Outline each blood parasite and name the species.
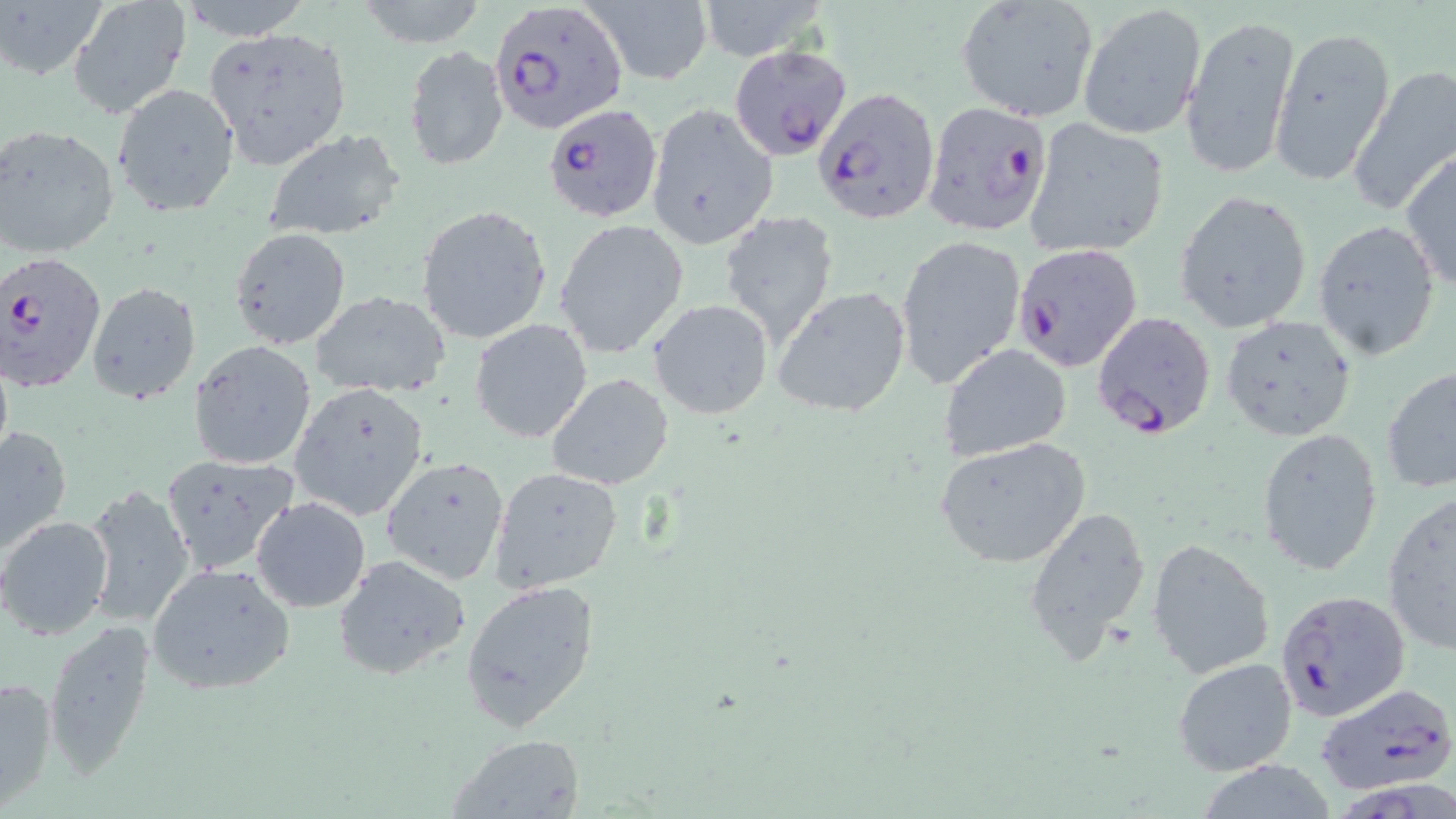

Approximate bounding boxes as named x1/y1/x2/y2 corners in pixels.
Plasmodium falciparum-infected red blood cells: (x1=492, y1=1, x2=628, y2=137), (x1=722, y1=42, x2=851, y2=167), (x1=811, y1=83, x2=941, y2=226), (x1=922, y1=99, x2=1054, y2=238), (x1=542, y1=104, x2=661, y2=222), (x1=1012, y1=242, x2=1143, y2=372), (x1=0, y1=251, x2=106, y2=393), (x1=1090, y1=310, x2=1217, y2=440), (x1=1275, y1=588, x2=1411, y2=722), (x1=1337, y1=771, x2=1456, y2=819).
No Plasmodium ovale, Plasmodium malariae, Plasmodium vivax, Babesia divergens, or Trypanosoma brucei observed.

slide-level diagnosis = Plasmodium falciparum
stain = May-Grünwald-Giemsa
magnification = 1000x
uninfected red blood cell locations = approximate bounding boxes as named x1/y1/x2/y2 corners in pixels: (x1=4, y1=0, x2=109, y2=82), (x1=67, y1=0, x2=192, y2=120), (x1=176, y1=0, x2=309, y2=38), (x1=353, y1=0, x2=491, y2=49), (x1=584, y1=0, x2=711, y2=86), (x1=695, y1=1, x2=829, y2=61), (x1=956, y1=1, x2=1099, y2=122), (x1=1077, y1=5, x2=1206, y2=141), (x1=1179, y1=11, x2=1301, y2=181), (x1=203, y1=26, x2=352, y2=170), (x1=1270, y1=26, x2=1395, y2=189), (x1=404, y1=45, x2=508, y2=171), (x1=1347, y1=66, x2=1456, y2=217), (x1=111, y1=82, x2=240, y2=216), (x1=646, y1=103, x2=778, y2=251), (x1=1023, y1=118, x2=1171, y2=259), (x1=0, y1=123, x2=121, y2=262), (x1=262, y1=129, x2=407, y2=242), (x1=1400, y1=150, x2=1456, y2=296), (x1=1174, y1=190, x2=1313, y2=334), (x1=416, y1=204, x2=551, y2=344), (x1=719, y1=213, x2=841, y2=352), (x1=555, y1=220, x2=690, y2=359), (x1=1312, y1=220, x2=1441, y2=361), (x1=229, y1=227, x2=352, y2=350), (x1=895, y1=233, x2=1027, y2=389), (x1=86, y1=282, x2=200, y2=406), (x1=772, y1=286, x2=913, y2=418), (x1=310, y1=291, x2=452, y2=399), (x1=649, y1=299, x2=776, y2=420), (x1=1220, y1=315, x2=1357, y2=440), (x1=470, y1=319, x2=594, y2=444), (x1=187, y1=339, x2=318, y2=471), (x1=937, y1=343, x2=1072, y2=462), (x1=1381, y1=365, x2=1456, y2=494), (x1=547, y1=373, x2=675, y2=491), (x1=287, y1=381, x2=432, y2=520), (x1=0, y1=424, x2=72, y2=556), (x1=1256, y1=428, x2=1384, y2=576), (x1=934, y1=437, x2=1092, y2=569), (x1=160, y1=453, x2=300, y2=576), (x1=379, y1=455, x2=510, y2=585), (x1=488, y1=466, x2=624, y2=593), (x1=81, y1=484, x2=196, y2=629), (x1=1381, y1=490, x2=1456, y2=656), (x1=251, y1=496, x2=371, y2=613), (x1=1023, y1=506, x2=1151, y2=664), (x1=0, y1=516, x2=114, y2=640), (x1=1146, y1=536, x2=1275, y2=679), (x1=333, y1=555, x2=473, y2=683), (x1=146, y1=561, x2=298, y2=696), (x1=459, y1=579, x2=601, y2=733), (x1=42, y1=619, x2=155, y2=778), (x1=1172, y1=656, x2=1297, y2=776), (x1=0, y1=675, x2=55, y2=810), (x1=1313, y1=681, x2=1456, y2=799), (x1=447, y1=733, x2=586, y2=818)
preparation = thin blood film
field of view = single
image size = 1456×819 pixels
modality = light microscopy